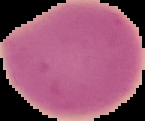

Summary:
  - Image size: 145×121 pixels
  - Image type: segmented cell region on a black background
  - Preparation: thin blood film
  - Malaria status: uninfected